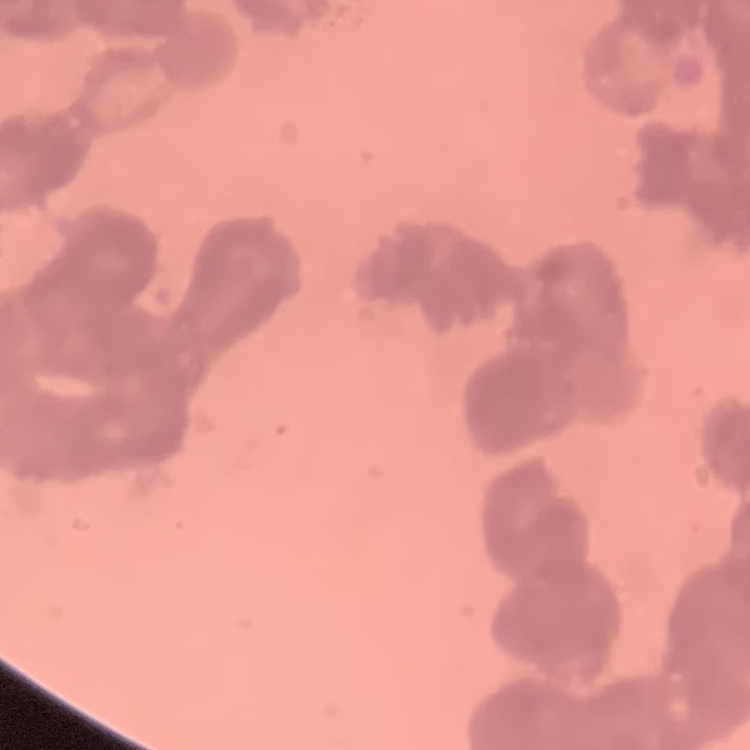
Summary:
  - Red blood cell morphology: rouleaux formation
  - Image type: one tile cut from a larger photomicrograph
  - Preparation: thin blood film
  - Stain: Field's or Giemsa